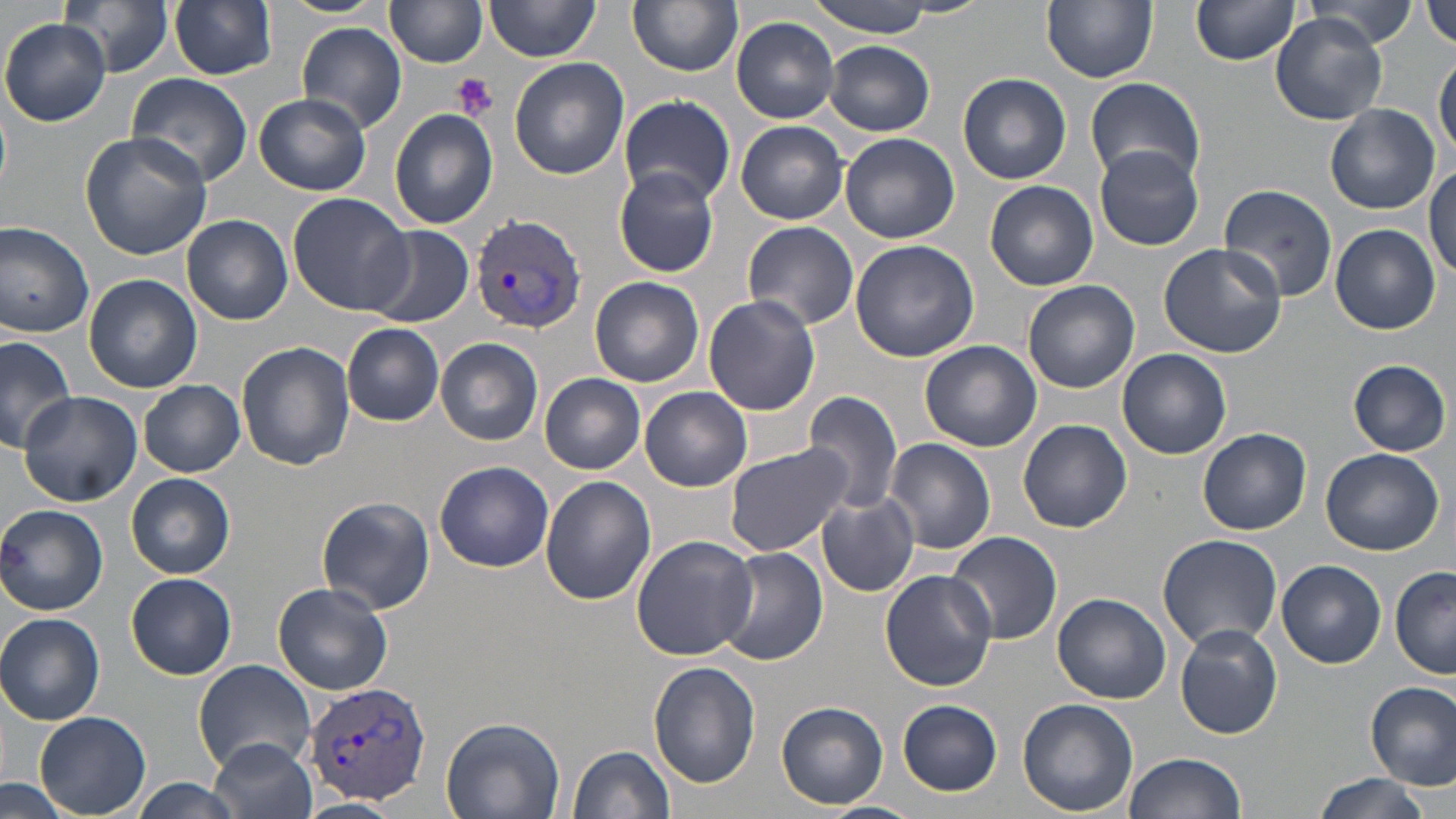

slide-level diagnosis = Plasmodium vivax
stain = May-Grünwald-Giemsa
field of view = single
uninfected red blood cell locations = approximate bounding boxes as (x1, y1, x2, y2) in pixels: (60, 0, 175, 76), (170, 0, 277, 80), (280, 0, 387, 19), (485, 0, 601, 62), (807, 0, 940, 38), (1042, 0, 1159, 84), (1191, 0, 1303, 67), (1425, 0, 1456, 50), (628, 1, 742, 76), (390, 2, 488, 68), (1299, 2, 1422, 48), (1268, 13, 1390, 124), (731, 16, 841, 123), (1, 17, 113, 127), (297, 24, 408, 134), (825, 41, 935, 136), (1434, 54, 1455, 159), (510, 58, 630, 181), (126, 72, 254, 190), (958, 73, 1072, 185), (1085, 75, 1205, 187), (254, 93, 372, 196), (619, 95, 735, 206), (1324, 104, 1439, 214), (389, 108, 498, 229), (736, 121, 848, 224), (80, 132, 212, 260), (840, 132, 960, 244), (1095, 144, 1204, 252), (1426, 162, 1456, 280), (613, 166, 721, 278), (986, 180, 1099, 291), (1217, 183, 1339, 302), (288, 192, 413, 315), (182, 214, 294, 325), (0, 219, 95, 339), (743, 220, 861, 330), (1331, 223, 1441, 334), (363, 225, 474, 329), (850, 238, 980, 361), (1158, 243, 1285, 357), (82, 273, 202, 393), (590, 275, 705, 387), (1023, 279, 1141, 395), (703, 295, 821, 415), (342, 323, 444, 425), (0, 335, 78, 456), (436, 338, 543, 445), (920, 339, 1042, 454), (236, 341, 355, 471), (1116, 349, 1232, 460), (1348, 360, 1451, 455), (539, 372, 645, 473), (139, 380, 246, 477), (641, 387, 753, 491), (17, 391, 141, 507), (805, 391, 901, 513), (1018, 418, 1133, 533), (1198, 429, 1312, 535), (885, 438, 996, 554), (725, 444, 853, 558), (1320, 447, 1445, 556), (434, 462, 554, 573), (127, 474, 236, 580), (540, 476, 657, 606), (817, 493, 919, 597), (315, 495, 435, 615), (0, 504, 109, 616), (945, 532, 1062, 646), (1157, 534, 1282, 650), (629, 535, 757, 661), (719, 545, 828, 666), (1278, 560, 1387, 669), (1391, 566, 1456, 679), (879, 568, 997, 691), (126, 573, 238, 681), (273, 582, 395, 696), (1053, 592, 1171, 704), (0, 613, 105, 724), (1175, 624, 1282, 739), (193, 659, 318, 773), (649, 661, 761, 789), (1366, 681, 1456, 790), (1017, 698, 1139, 815), (897, 699, 1003, 795), (776, 702, 888, 809), (34, 711, 152, 817), (441, 716, 565, 819), (209, 736, 316, 819), (567, 745, 676, 819), (1125, 751, 1247, 818), (1310, 774, 1434, 819), (129, 779, 245, 819), (0, 780, 73, 819), (296, 798, 403, 819), (813, 801, 924, 819)
image size = 1456×819 pixels
magnification = 1000x
modality = light microscopy
preparation = thin blood smear
Plasmodium vivax-infected red blood cell locations = approximate bounding boxes as (x1, y1, x2, y2) in pixels: (470, 214, 588, 332), (305, 680, 432, 805)
platelet locations = approximate bounding boxes as (x1, y1, x2, y2) in pixels: (450, 73, 499, 120)